Report the malaria status of this cell.
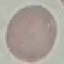

It is uninfected.

Summary:
  - Preparation: thin smear
  - Capture: smartphone through the microscope eyepiece
  - Image type: cell patch, automatically extracted from a larger field of view and resized to 64 × 64 pixels
  - Stain: Giemsa